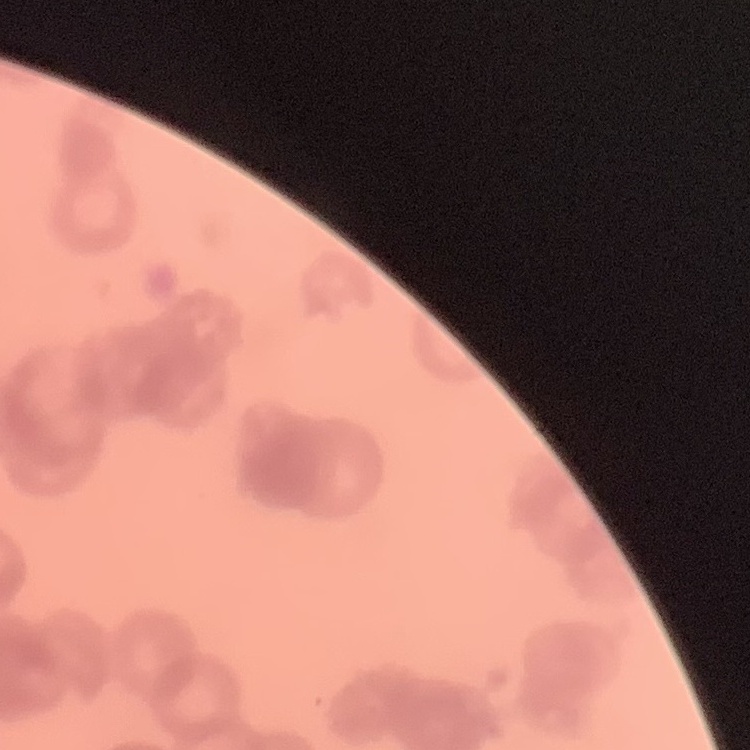
Summary:
  - Red blood cell morphology: rouleaux formation
  - Stain: Field's or Giemsa
  - Image type: one tile cut from a larger photomicrograph
  - Preparation: thin blood film